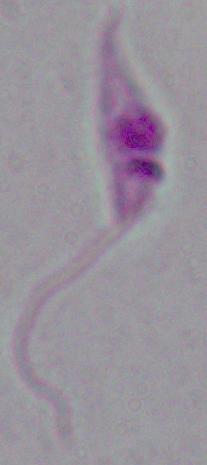
Summary:
  - Magnification: 1000x
  - Identification: Leishmania
  - Modality: micrograph